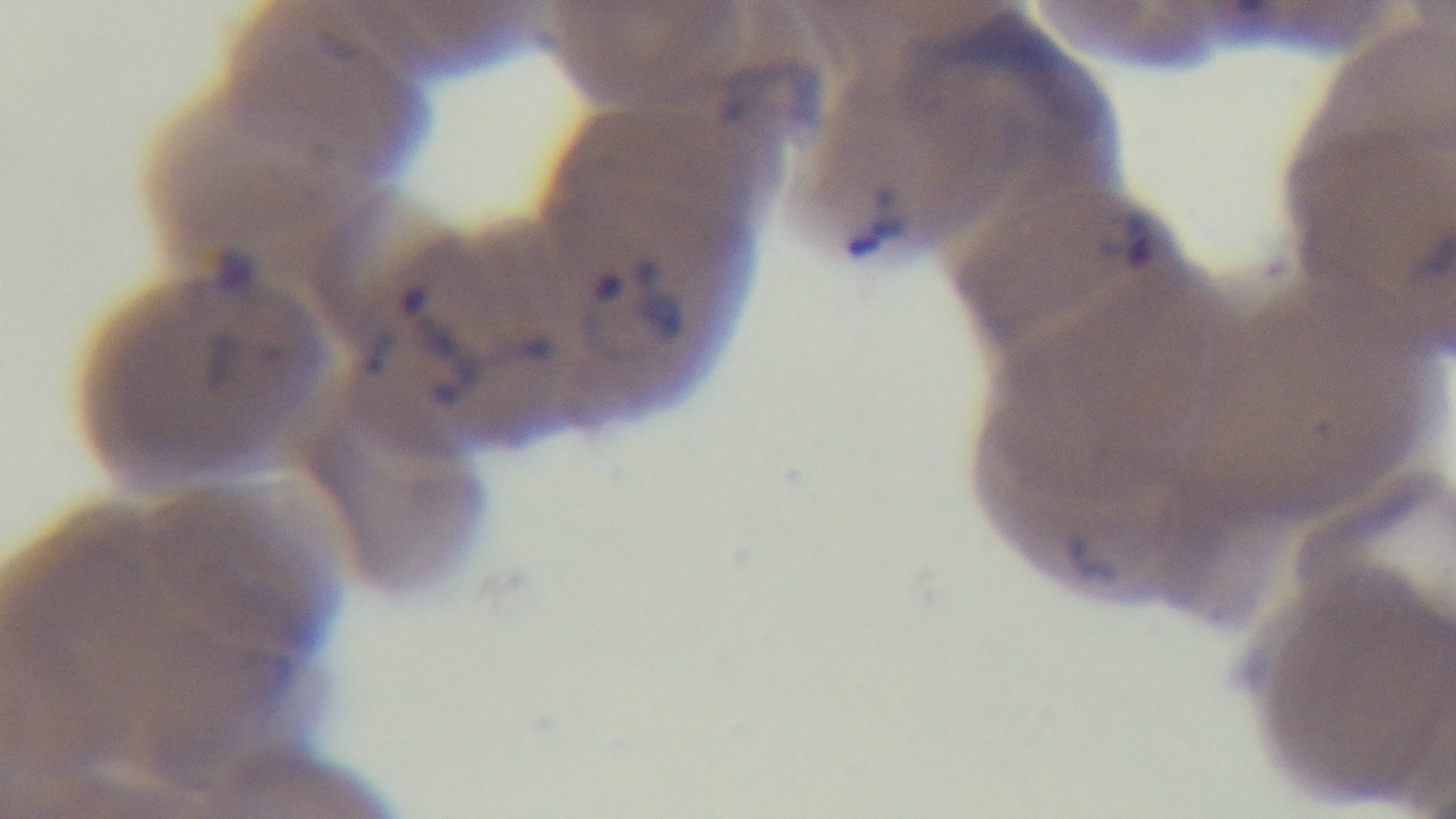 Photomicrograph. Single field of view. Giemsa-stained. Oil-immersion objective, 100x. Captured with a mounted 4K digital camera. Malaria status: positive. Preparation: thin.